State the blood parasite species.
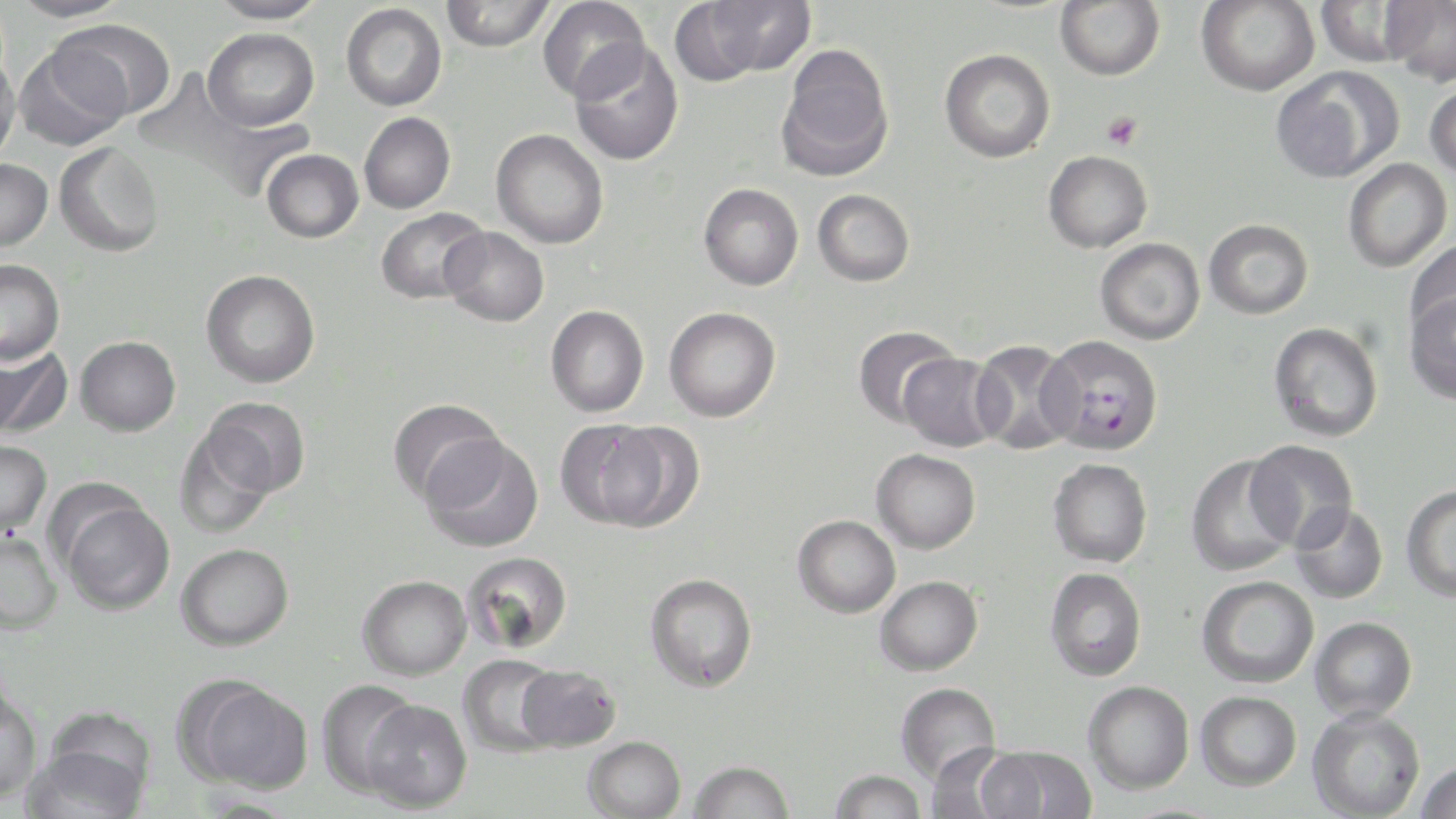

Plasmodium falciparum.

platelet locations = approximate bounding boxes as named x1/y1/x2/y2 corners in pixels: (x1=1101, y1=111, x2=1142, y2=151)
preparation = thin blood film
modality = light microscopy
Plasmodium falciparum-infected red blood cell locations = approximate bounding boxes as named x1/y1/x2/y2 corners in pixels: (x1=1039, y1=334, x2=1164, y2=456)
uninfected red blood cell locations = approximate bounding boxes as named x1/y1/x2/y2 corners in pixels: (x1=10, y1=0, x2=131, y2=23), (x1=208, y1=0, x2=327, y2=25), (x1=440, y1=0, x2=555, y2=51), (x1=537, y1=0, x2=650, y2=102), (x1=696, y1=0, x2=816, y2=79), (x1=1380, y1=0, x2=1456, y2=85), (x1=1055, y1=1, x2=1165, y2=80), (x1=1197, y1=1, x2=1320, y2=96), (x1=1313, y1=1, x2=1418, y2=67), (x1=341, y1=3, x2=447, y2=111), (x1=52, y1=19, x2=176, y2=122), (x1=202, y1=27, x2=319, y2=131), (x1=14, y1=42, x2=130, y2=150), (x1=569, y1=42, x2=685, y2=166), (x1=777, y1=42, x2=894, y2=179), (x1=939, y1=48, x2=1056, y2=163), (x1=0, y1=50, x2=20, y2=165), (x1=1271, y1=67, x2=1403, y2=184), (x1=1425, y1=80, x2=1456, y2=182), (x1=359, y1=112, x2=455, y2=213), (x1=491, y1=129, x2=609, y2=249), (x1=54, y1=142, x2=164, y2=257), (x1=261, y1=149, x2=363, y2=243), (x1=1043, y1=150, x2=1153, y2=253), (x1=0, y1=158, x2=52, y2=251), (x1=1343, y1=159, x2=1452, y2=272), (x1=698, y1=183, x2=804, y2=291), (x1=812, y1=189, x2=915, y2=287), (x1=375, y1=207, x2=490, y2=304), (x1=1204, y1=218, x2=1314, y2=319), (x1=440, y1=226, x2=549, y2=327), (x1=1095, y1=238, x2=1205, y2=345), (x1=1405, y1=239, x2=1456, y2=341), (x1=0, y1=259, x2=65, y2=365), (x1=201, y1=269, x2=320, y2=388), (x1=1403, y1=290, x2=1456, y2=406), (x1=545, y1=305, x2=649, y2=417), (x1=664, y1=307, x2=781, y2=422), (x1=1268, y1=322, x2=1383, y2=443), (x1=854, y1=325, x2=959, y2=428), (x1=75, y1=336, x2=180, y2=436), (x1=969, y1=340, x2=1081, y2=454), (x1=0, y1=341, x2=72, y2=440), (x1=898, y1=353, x2=1005, y2=452), (x1=202, y1=397, x2=310, y2=498), (x1=388, y1=398, x2=505, y2=505), (x1=554, y1=419, x2=664, y2=528), (x1=595, y1=421, x2=706, y2=532), (x1=172, y1=427, x2=279, y2=537), (x1=420, y1=435, x2=545, y2=553), (x1=1245, y1=439, x2=1358, y2=547), (x1=0, y1=440, x2=51, y2=536), (x1=871, y1=448, x2=981, y2=553), (x1=1185, y1=455, x2=1300, y2=577), (x1=1047, y1=458, x2=1153, y2=568), (x1=1401, y1=484, x2=1456, y2=602), (x1=58, y1=496, x2=174, y2=615), (x1=1289, y1=502, x2=1389, y2=604), (x1=792, y1=514, x2=901, y2=618), (x1=0, y1=528, x2=63, y2=633), (x1=176, y1=543, x2=293, y2=650), (x1=462, y1=551, x2=573, y2=655), (x1=1044, y1=567, x2=1147, y2=681), (x1=644, y1=572, x2=758, y2=693), (x1=357, y1=575, x2=471, y2=680), (x1=875, y1=575, x2=983, y2=676), (x1=1196, y1=575, x2=1319, y2=688), (x1=1309, y1=616, x2=1417, y2=722), (x1=457, y1=654, x2=564, y2=758), (x1=517, y1=664, x2=621, y2=751), (x1=183, y1=678, x2=314, y2=793), (x1=315, y1=680, x2=423, y2=797), (x1=1083, y1=680, x2=1194, y2=794), (x1=895, y1=682, x2=1001, y2=782), (x1=0, y1=683, x2=43, y2=804), (x1=1195, y1=690, x2=1302, y2=790), (x1=362, y1=699, x2=473, y2=813), (x1=1307, y1=706, x2=1425, y2=818), (x1=25, y1=716, x2=153, y2=819), (x1=582, y1=735, x2=686, y2=819), (x1=924, y1=743, x2=1026, y2=819), (x1=977, y1=744, x2=1096, y2=818), (x1=686, y1=759, x2=795, y2=819), (x1=1415, y1=760, x2=1456, y2=819), (x1=828, y1=768, x2=927, y2=818), (x1=194, y1=795, x2=300, y2=818)
field of view = single
stain = May-Grünwald-Giemsa
magnification = 1000x
image size = 1456×819 pixels